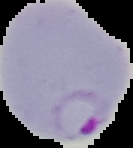
Summary:
  - Preparation: thin blood film
  - Result: Plasmodium parasites detected
  - Image size: 133×148 pixels
  - Image type: segmented cell region on a black background